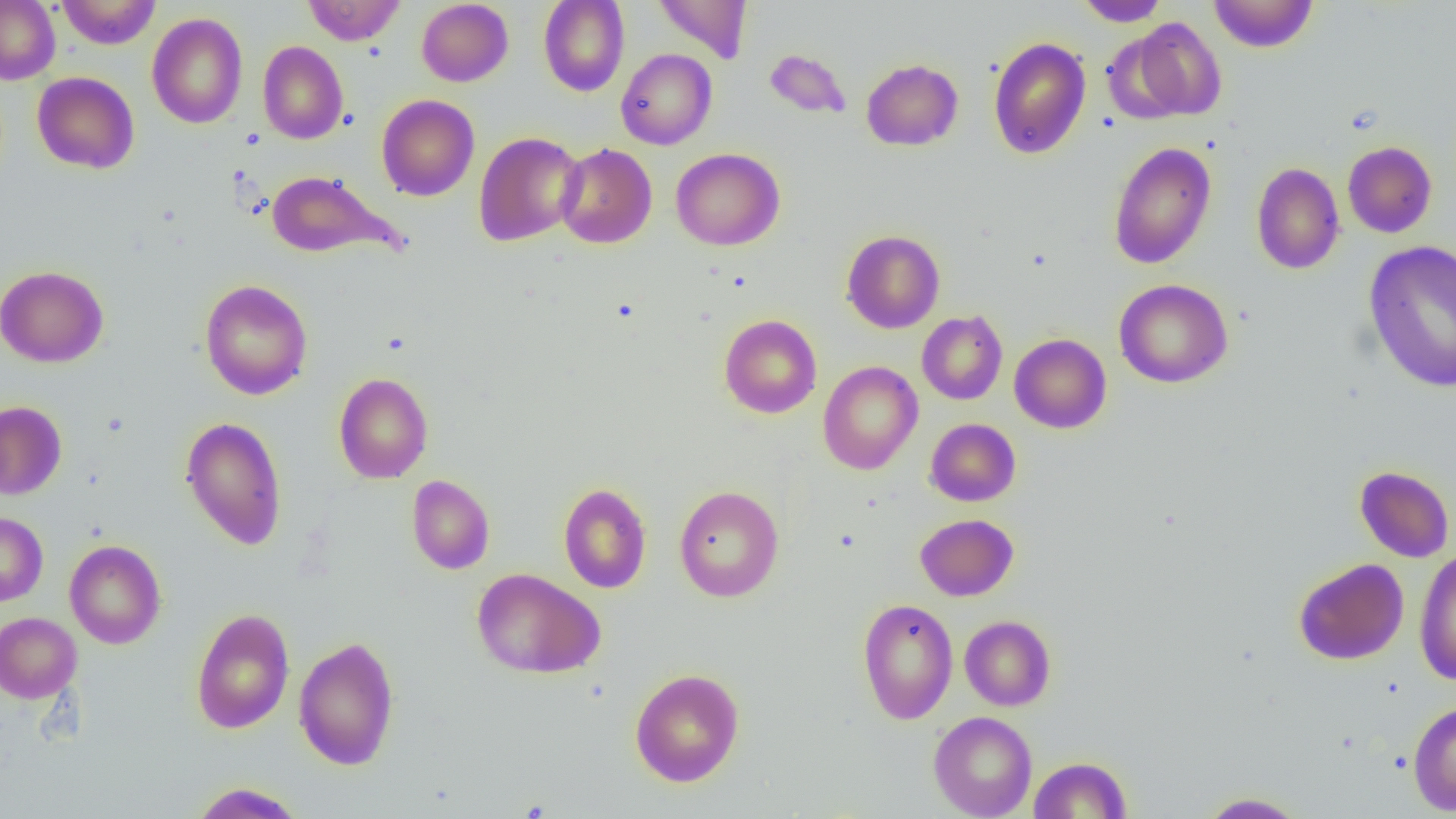
Approximate bounding boxes as named x1/y1/x2/y2 corners in pixels. Uninfected red blood cell locations: (x1=0, y1=0, x2=60, y2=84), (x1=56, y1=0, x2=161, y2=49), (x1=302, y1=0, x2=405, y2=45), (x1=416, y1=0, x2=513, y2=86), (x1=654, y1=0, x2=752, y2=63), (x1=1076, y1=0, x2=1168, y2=26), (x1=1209, y1=0, x2=1318, y2=53), (x1=538, y1=1, x2=630, y2=96), (x1=146, y1=11, x2=247, y2=129), (x1=1125, y1=17, x2=1227, y2=122), (x1=988, y1=36, x2=1091, y2=159), (x1=258, y1=41, x2=348, y2=144), (x1=616, y1=49, x2=717, y2=150), (x1=764, y1=49, x2=851, y2=119), (x1=861, y1=58, x2=963, y2=150), (x1=32, y1=72, x2=139, y2=174), (x1=376, y1=94, x2=480, y2=201), (x1=473, y1=131, x2=586, y2=247), (x1=1342, y1=141, x2=1437, y2=238), (x1=1108, y1=142, x2=1217, y2=269), (x1=555, y1=143, x2=657, y2=248), (x1=670, y1=148, x2=785, y2=250), (x1=1251, y1=162, x2=1344, y2=274), (x1=265, y1=170, x2=403, y2=260), (x1=841, y1=230, x2=945, y2=333), (x1=1363, y1=241, x2=1456, y2=394), (x1=0, y1=265, x2=108, y2=368), (x1=199, y1=279, x2=313, y2=400), (x1=1114, y1=279, x2=1234, y2=388), (x1=917, y1=310, x2=1008, y2=405), (x1=719, y1=314, x2=822, y2=419), (x1=1009, y1=333, x2=1112, y2=433), (x1=818, y1=360, x2=923, y2=475), (x1=333, y1=372, x2=433, y2=484), (x1=0, y1=400, x2=67, y2=500), (x1=180, y1=416, x2=288, y2=551), (x1=925, y1=418, x2=1021, y2=506), (x1=1354, y1=466, x2=1454, y2=562), (x1=407, y1=475, x2=495, y2=574), (x1=559, y1=483, x2=651, y2=594), (x1=673, y1=485, x2=784, y2=602), (x1=0, y1=512, x2=48, y2=606), (x1=915, y1=514, x2=1018, y2=601), (x1=65, y1=540, x2=166, y2=649), (x1=1414, y1=548, x2=1455, y2=685), (x1=1293, y1=557, x2=1409, y2=665), (x1=472, y1=567, x2=604, y2=679), (x1=857, y1=598, x2=958, y2=724), (x1=190, y1=607, x2=295, y2=734), (x1=0, y1=612, x2=81, y2=703), (x1=960, y1=615, x2=1055, y2=711), (x1=293, y1=636, x2=401, y2=771), (x1=629, y1=667, x2=744, y2=787), (x1=1408, y1=699, x2=1456, y2=816), (x1=928, y1=711, x2=1037, y2=819), (x1=1029, y1=756, x2=1131, y2=818), (x1=189, y1=782, x2=307, y2=819), (x1=1198, y1=791, x2=1308, y2=818). Slide-level diagnosis: negative for blood parasites. Light microscopy. Image is 1456×819 pixels. Thin blood smear. Captured at 1000x magnification. Single field of view.